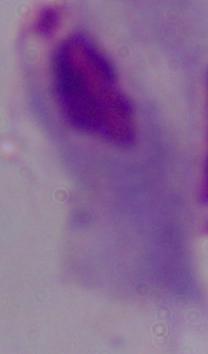

modality = photomicrograph
magnification = 1000x
identification = trichomonad